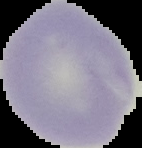
Summary:
  - Malaria status: uninfected
  - Image size: 142×148 pixels
  - Preparation: thin blood smear
  - Image type: segmented cell region with the area outside set to black